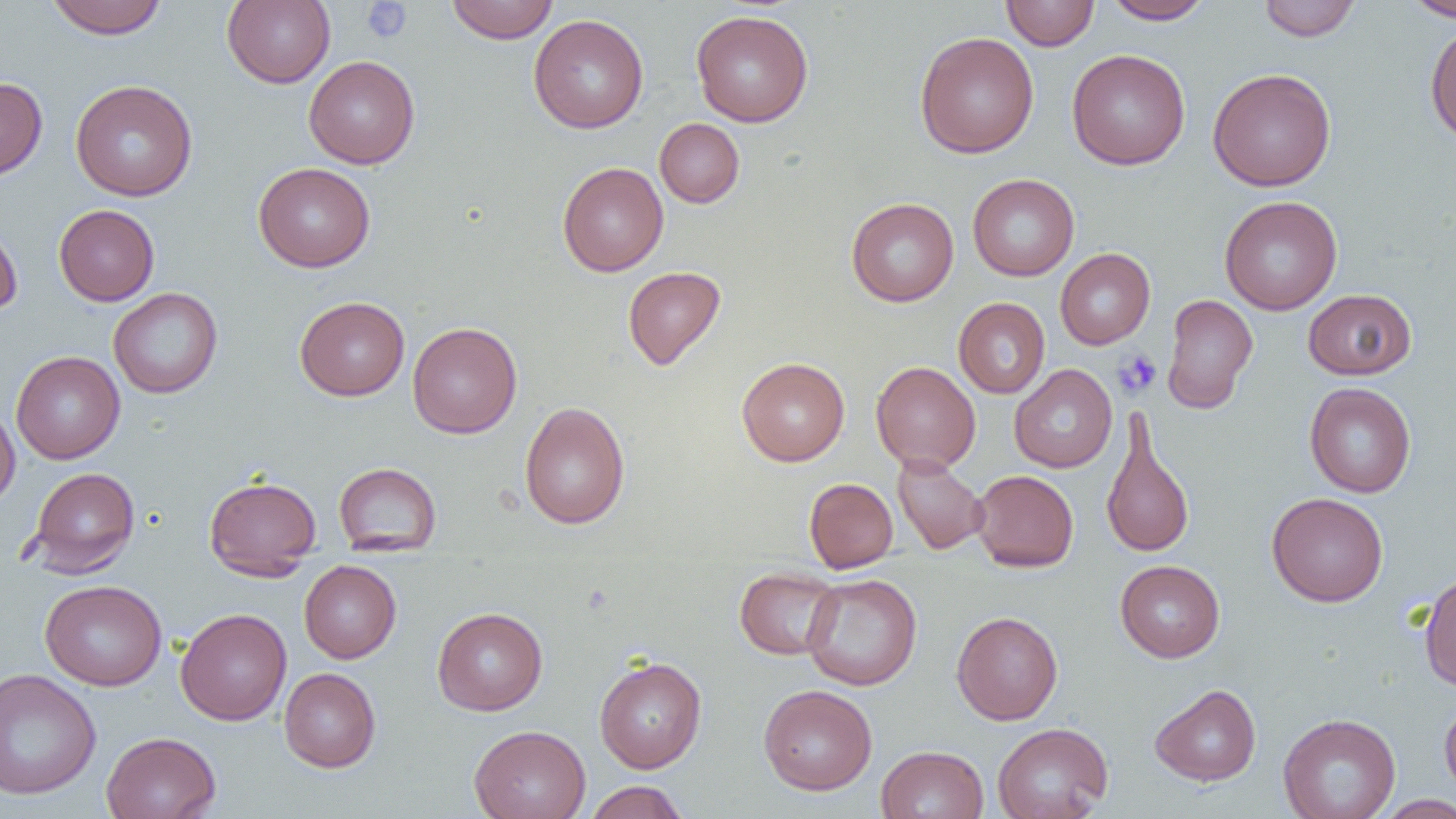

Summary:
  - Coordinate format: approximate bounding boxes as named x1/y1/x2/y2 corners in pixels
  - Platelet locations: (x1=361, y1=1, x2=412, y2=43), (x1=1113, y1=348, x2=1161, y2=398)
  - Uninfected red blood cell locations: (x1=44, y1=0, x2=169, y2=39), (x1=222, y1=0, x2=336, y2=89), (x1=446, y1=0, x2=558, y2=43), (x1=1001, y1=0, x2=1099, y2=51), (x1=1102, y1=0, x2=1213, y2=24), (x1=1257, y1=0, x2=1362, y2=41), (x1=1403, y1=0, x2=1456, y2=21), (x1=691, y1=10, x2=813, y2=127), (x1=529, y1=14, x2=649, y2=134), (x1=1425, y1=22, x2=1456, y2=144), (x1=914, y1=31, x2=1039, y2=158), (x1=1067, y1=49, x2=1190, y2=170), (x1=304, y1=55, x2=419, y2=169), (x1=1207, y1=68, x2=1337, y2=191), (x1=0, y1=77, x2=47, y2=181), (x1=70, y1=79, x2=198, y2=201), (x1=655, y1=118, x2=744, y2=208), (x1=557, y1=161, x2=668, y2=276), (x1=253, y1=162, x2=375, y2=272), (x1=968, y1=173, x2=1079, y2=281), (x1=1220, y1=195, x2=1343, y2=315), (x1=846, y1=197, x2=959, y2=306), (x1=54, y1=204, x2=159, y2=305), (x1=0, y1=217, x2=23, y2=319), (x1=1055, y1=248, x2=1155, y2=349), (x1=622, y1=266, x2=726, y2=370), (x1=108, y1=287, x2=223, y2=398), (x1=1302, y1=289, x2=1417, y2=380), (x1=1162, y1=294, x2=1258, y2=413), (x1=295, y1=296, x2=410, y2=400), (x1=953, y1=297, x2=1050, y2=398), (x1=407, y1=321, x2=522, y2=439), (x1=11, y1=351, x2=125, y2=463), (x1=736, y1=357, x2=850, y2=466), (x1=870, y1=361, x2=981, y2=473), (x1=1009, y1=365, x2=1117, y2=472), (x1=1304, y1=382, x2=1416, y2=498), (x1=519, y1=401, x2=630, y2=529), (x1=0, y1=402, x2=20, y2=509), (x1=1100, y1=414, x2=1196, y2=560), (x1=892, y1=454, x2=990, y2=555), (x1=334, y1=462, x2=442, y2=555), (x1=28, y1=466, x2=139, y2=577), (x1=970, y1=470, x2=1079, y2=572), (x1=204, y1=474, x2=322, y2=579), (x1=804, y1=478, x2=898, y2=573), (x1=1267, y1=492, x2=1388, y2=607), (x1=299, y1=560, x2=401, y2=663), (x1=1114, y1=560, x2=1225, y2=662), (x1=734, y1=567, x2=842, y2=660), (x1=1419, y1=571, x2=1456, y2=691), (x1=802, y1=573, x2=922, y2=691), (x1=40, y1=580, x2=167, y2=690), (x1=432, y1=606, x2=547, y2=715), (x1=175, y1=608, x2=292, y2=725), (x1=951, y1=611, x2=1063, y2=725), (x1=594, y1=656, x2=707, y2=773), (x1=279, y1=667, x2=381, y2=772), (x1=0, y1=668, x2=101, y2=800), (x1=758, y1=684, x2=877, y2=795), (x1=1150, y1=684, x2=1261, y2=786), (x1=1440, y1=696, x2=1456, y2=800), (x1=1278, y1=713, x2=1401, y2=819), (x1=992, y1=722, x2=1113, y2=819), (x1=469, y1=724, x2=591, y2=819), (x1=101, y1=731, x2=221, y2=819), (x1=876, y1=745, x2=989, y2=819), (x1=583, y1=781, x2=690, y2=819), (x1=1375, y1=794, x2=1456, y2=818)
  - Slide-level diagnosis: no evidence of blood parasites
  - Preparation: thin blood film
  - Modality: light microscopy
  - Magnification: 1000x
  - Field of view: single
  - Image size: 1456×819 pixels